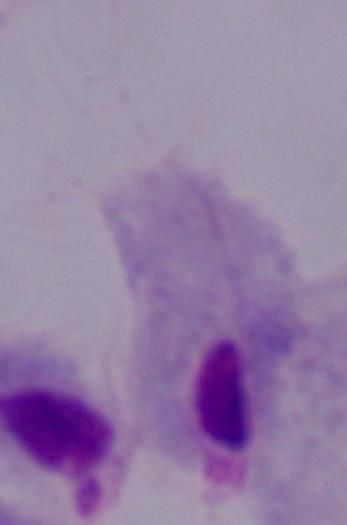

A trichomonad is shown. Photomicrograph. 1000x magnification.